Name the parasite shown.
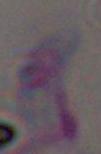

Toxoplasma gondii.

1000x magnification. Micrograph.